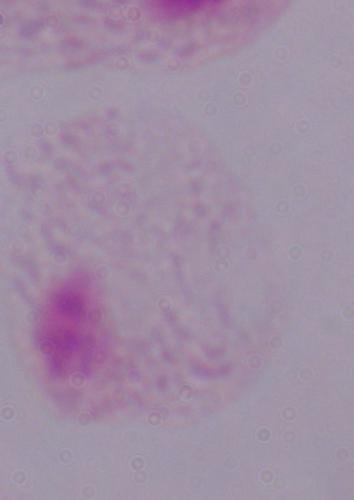

modality = micrograph
magnification = 1000x
identification = trichomonad